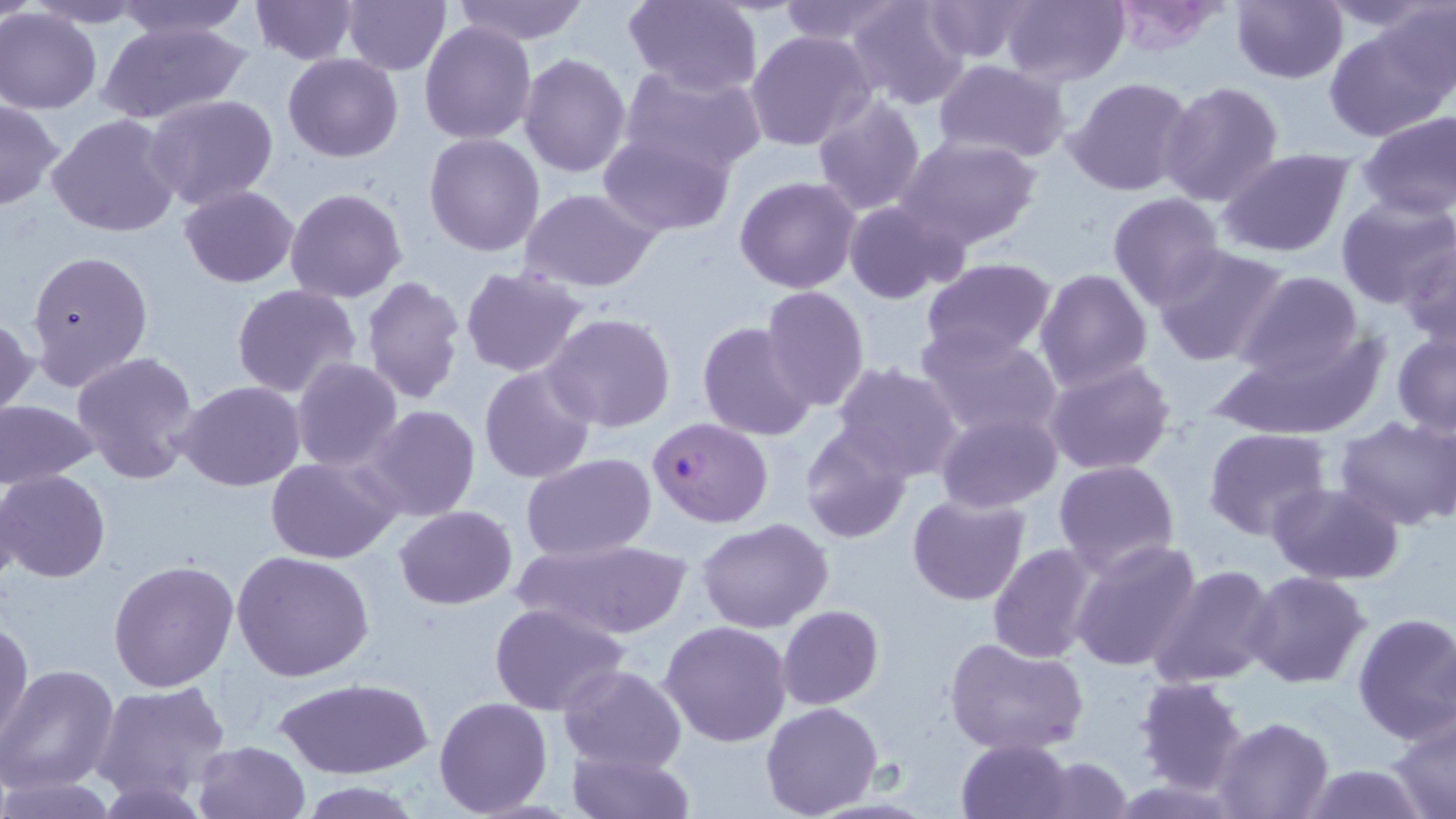
Summary:
  - Coordinate format: approximate bounding boxes as (x1,y1)-(x2,y2) corner pairs in pixels
  - Uninfected red blood cell locations: (0,0)-(37,28), (22,0)-(152,28), (106,0)-(252,41), (248,0)-(361,66), (341,0)-(451,76), (624,0)-(764,96), (776,0)-(907,45), (844,0)-(971,110), (922,0)-(1035,62), (1000,0)-(1131,86), (1109,0)-(1233,53), (1229,0)-(1348,85), (1368,0)-(1456,111), (452,1)-(592,44), (1,8)-(103,114), (1326,16)-(1454,142), (97,18)-(249,127), (419,21)-(537,145), (744,31)-(875,151), (283,52)-(402,163), (518,52)-(632,177), (933,60)-(1072,163), (621,67)-(769,173), (1064,76)-(1195,197), (1159,80)-(1285,207), (144,93)-(278,210), (811,95)-(927,215), (0,99)-(64,211), (1357,110)-(1456,221), (47,114)-(181,240), (599,133)-(737,237), (424,134)-(546,258), (896,135)-(1042,249), (1214,149)-(1356,258), (734,176)-(861,294), (179,186)-(299,288), (284,187)-(409,305), (520,188)-(660,293), (1107,193)-(1227,311), (1334,197)-(1455,310), (843,198)-(962,304), (1397,232)-(1456,348), (1150,243)-(1291,365), (26,249)-(154,390), (921,258)-(1057,363), (1034,266)-(1153,394), (459,267)-(589,379), (1234,270)-(1366,381), (361,276)-(467,403), (231,283)-(362,401), (758,285)-(869,412), (542,313)-(678,433), (1,314)-(36,418), (697,322)-(819,441), (915,326)-(1065,443), (1212,328)-(1389,441), (1390,329)-(1456,437), (70,351)-(200,485), (290,358)-(404,473), (1044,358)-(1176,477), (833,360)-(963,482), (479,365)-(596,483), (177,380)-(305,493), (0,400)-(100,489), (363,405)-(480,523), (936,411)-(1063,513), (1334,415)-(1456,531), (799,422)-(915,542), (1203,428)-(1332,541), (521,452)-(657,563), (266,455)-(403,565), (1053,458)-(1180,573), (1,470)-(111,583), (1,473)-(28,591), (1269,482)-(1405,584), (907,493)-(1031,605), (394,505)-(518,609), (697,519)-(832,633), (512,537)-(693,638), (1068,538)-(1202,671), (988,544)-(1100,662), (232,551)-(375,681), (108,557)-(239,692), (1149,564)-(1280,688), (1242,571)-(1370,690), (487,602)-(630,716), (778,605)-(883,709), (1351,611)-(1456,744), (0,617)-(33,748), (660,621)-(793,747), (944,636)-(1089,756), (557,664)-(687,776), (0,665)-(121,794), (1134,674)-(1250,795), (274,677)-(430,779), (92,680)-(231,802), (433,697)-(553,817), (761,702)-(885,819), (1387,709)-(1456,818), (1212,717)-(1332,819), (956,738)-(1075,819), (193,740)-(311,819), (565,745)-(694,819), (1036,757)-(1134,817), (1295,763)-(1431,819), (2,777)-(120,818), (296,779)-(425,817)
  - Plasmodium falciparum-infected red blood cell locations: (648,417)-(775,528)
  - Slide-level diagnosis: Plasmodium falciparum
  - Field of view: one of a larger specimen
  - Image size: 1456×819 pixels
  - Preparation: thin blood film
  - Modality: light microscopy
  - Stain: May-Grünwald-Giemsa
  - Magnification: 1000x